Classify this cell by malaria status.
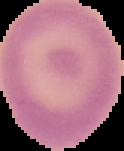

Uninfected.

image size = 124×151 pixels
preparation = thin blood smear
image type = segmented cell region on a black background